Locate every uninfected red blood cell.
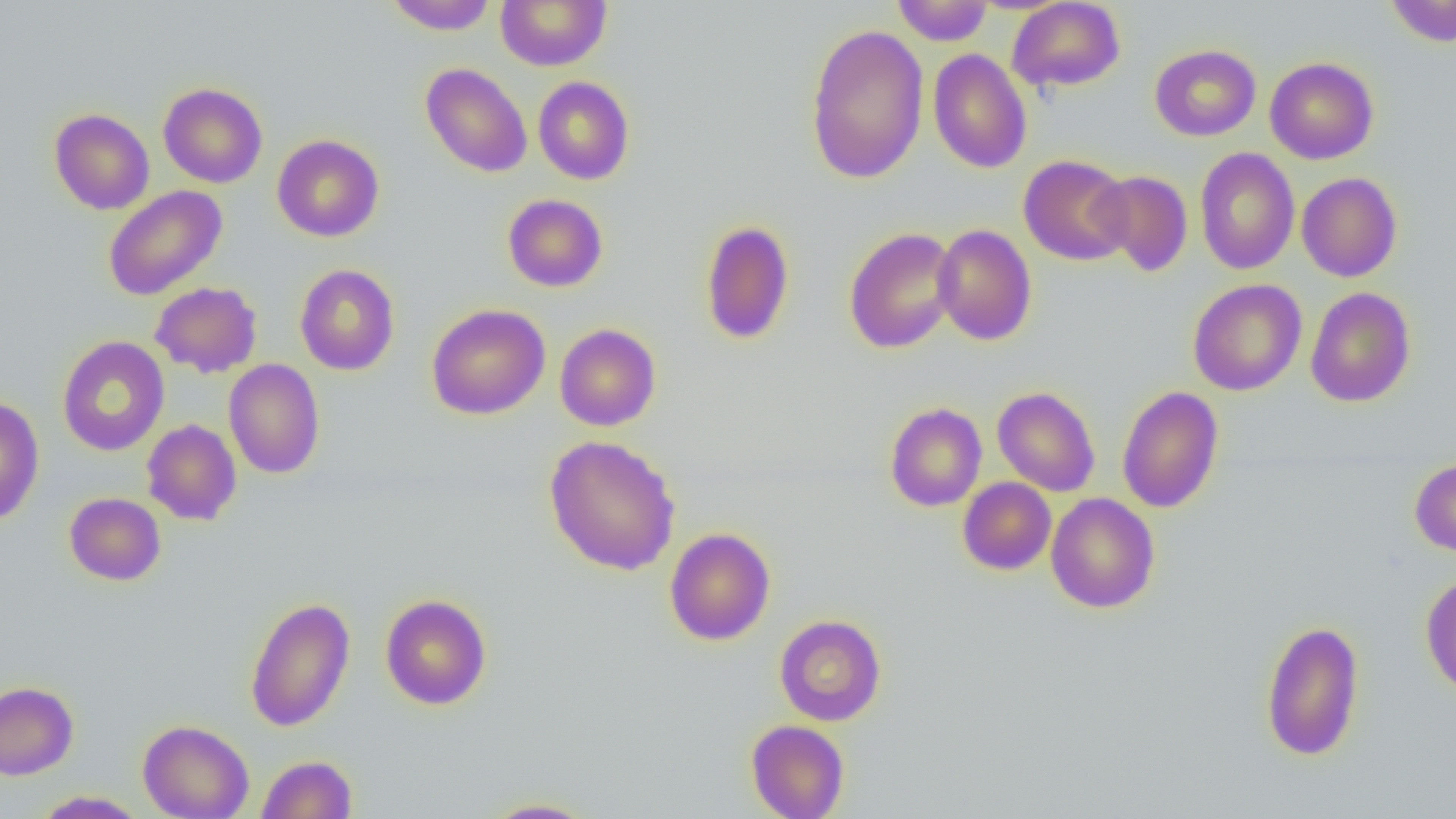

Approximate bounding boxes as [x1, y1, x2, y2] in pixels.
Uninfected red blood cells: [383, 0, 499, 34], [495, 0, 611, 71], [1385, 0, 1456, 47], [892, 1, 993, 45], [1007, 1, 1125, 92], [805, 23, 929, 184], [1149, 44, 1261, 141], [928, 48, 1032, 174], [1149, 50, 1379, 146], [1264, 57, 1379, 164], [420, 62, 532, 177], [533, 76, 634, 185], [158, 82, 267, 188], [49, 108, 154, 214], [271, 134, 384, 242], [1194, 147, 1300, 275], [1018, 154, 1133, 266], [1091, 170, 1193, 276], [1296, 172, 1402, 282], [102, 185, 227, 301], [502, 193, 608, 292], [700, 220, 795, 345], [932, 224, 1037, 345], [843, 227, 959, 354], [294, 263, 400, 375], [1188, 278, 1306, 396], [150, 281, 263, 378], [1305, 286, 1416, 407], [426, 303, 550, 420], [554, 323, 661, 431], [57, 336, 169, 457], [223, 358, 325, 479], [992, 386, 1101, 497], [1116, 386, 1224, 514], [0, 396, 45, 526], [884, 402, 987, 512], [142, 419, 242, 526], [544, 435, 681, 576], [1410, 458, 1456, 557], [958, 477, 1056, 575], [64, 493, 166, 586], [1045, 493, 1160, 613], [664, 527, 776, 646], [1420, 572, 1456, 696], [380, 594, 492, 710], [244, 596, 356, 733], [774, 614, 886, 726], [1260, 618, 1365, 762], [0, 681, 79, 780], [137, 719, 254, 819], [746, 720, 849, 819], [256, 754, 358, 819], [33, 790, 147, 818], [478, 797, 599, 818].

slide-level diagnosis = no evidence of blood parasites
magnification = 1000x
field of view = one of a larger specimen
preparation = thin blood smear
modality = light microscopy
image size = 1456×819 pixels